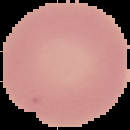

The area outside the segmented cell region is set to black. Result: no Plasmodium parasites detected. From a thin blood film. Image is 130×130 pixels.